Give the preparation type.
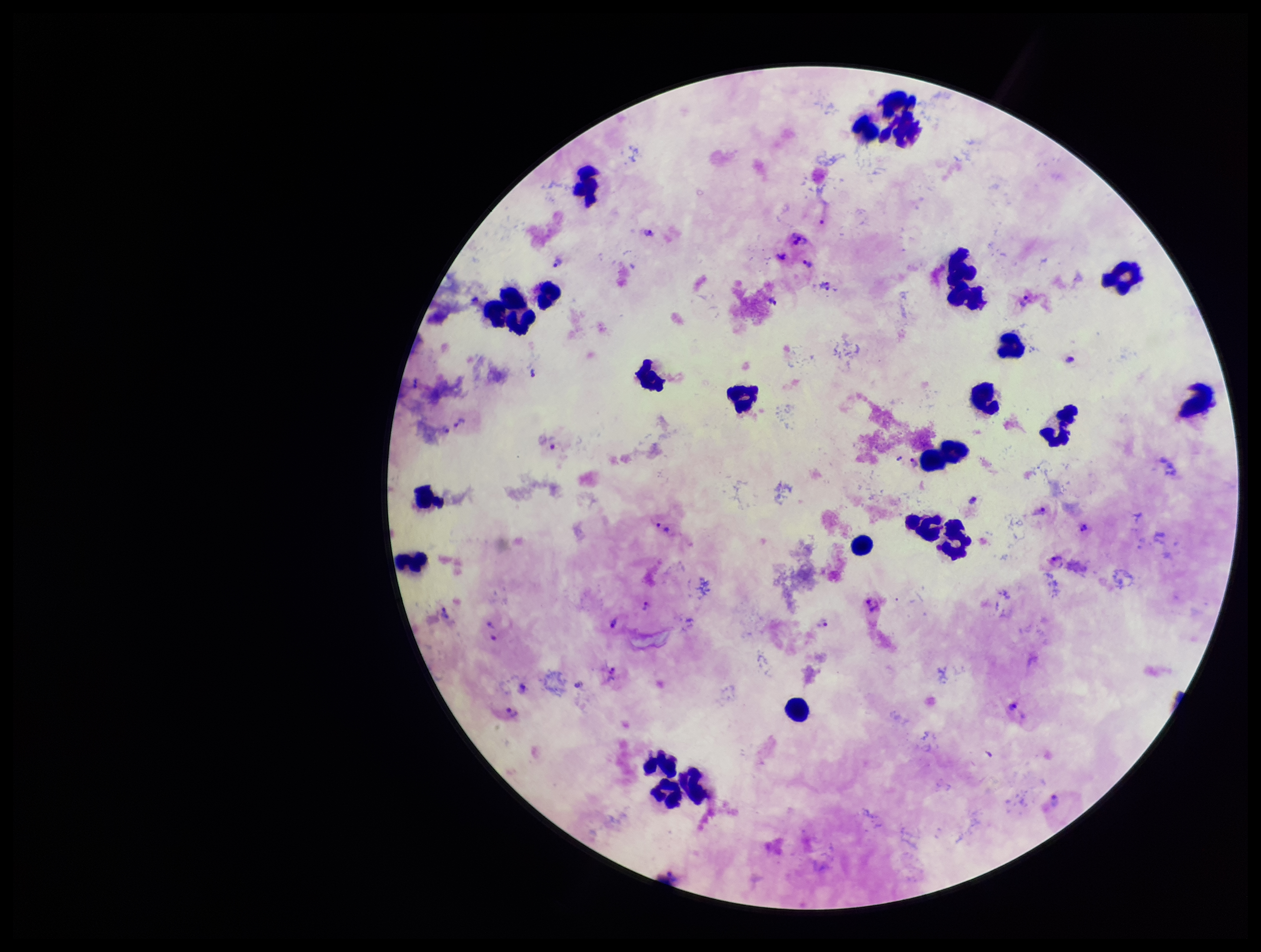
It is a thick blood smear.

Summary:
  - Species reported for this patient: Plasmodium vivax
  - Image size: 1261×952 pixels
  - Capture: smartphone photograph through the microscope eyepiece
  - Parasite count: 20
  - Plasmodium parasites: identified
  - Leukocyte count: 27
  - Patient malaria status: positive
  - Stain: Giemsa
  - Field of view: single